Identify the blood parasite species.
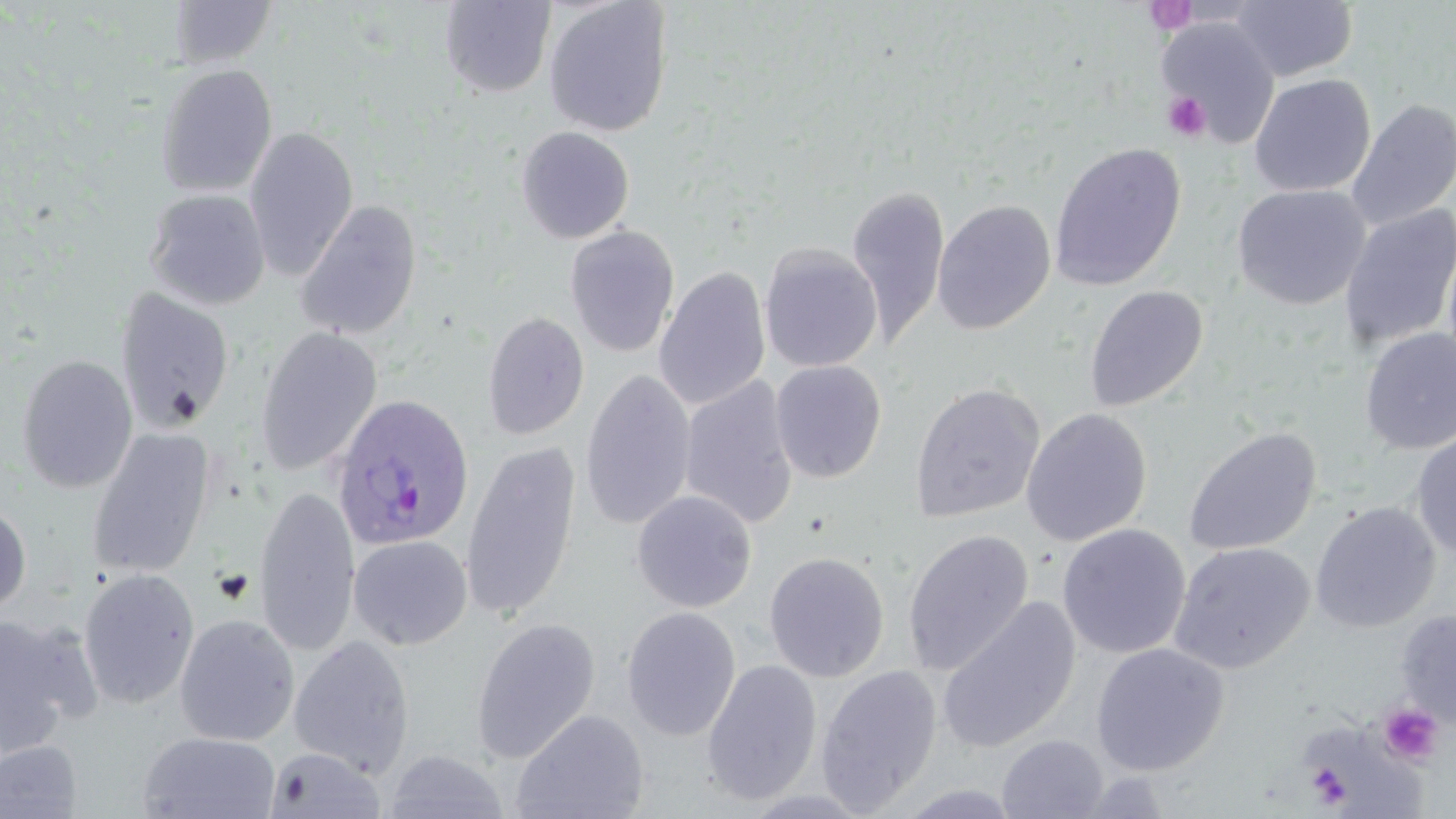

Plasmodium ovale.

image_size: 1456×819 pixels
magnification: 1000x
plasmodium_ovale_infected_red_blood_cell_locations: 'approximate bounding boxes as (x1,y1)-(x2,y2) corner pairs in pixels: (331,393)-(475,552)'
stain: May-Grünwald-Giemsa
preparation: thin blood film
platelet_locations: 'approximate bounding boxes as (x1,y1)-(x2,y2) corner pairs in pixels: (1163,91)-(1211,143), (1378,703)-(1444,765), (1305,762)-(1354,808)'
field_of_view: single
modality: light microscopy
uninfected_red_blood_cell_locations: 'approximate bounding boxes as (x1,y1)-(x2,y2) corner pairs in pixels: (439,0)-(556,98), (168,1)-(277,68), (543,1)-(673,138), (1229,1)-(1358,81), (1157,18)-(1279,146), (155,64)-(277,198), (1249,73)-(1375,197), (1346,98)-(1456,231), (244,126)-(358,282), (515,126)-(635,244), (1049,142)-(1187,292), (846,182)-(950,351), (1232,184)-(1371,310), (144,189)-(271,310), (932,199)-(1056,335), (295,200)-(423,340), (1338,205)-(1456,350), (565,226)-(681,358), (1442,234)-(1456,382), (758,242)-(883,373), (653,265)-(771,412), (1084,285)-(1209,412), (114,288)-(236,435), (481,310)-(589,441), (254,327)-(383,477), (1359,329)-(1456,455), (16,355)-(138,493), (770,360)-(887,483), (580,369)-(697,531), (679,375)-(800,529), (909,381)-(1046,523), (1021,407)-(1153,546), (1182,426)-(1322,557), (86,428)-(215,579), (1410,433)-(1456,560), (460,441)-(581,621), (254,485)-(360,658), (631,490)-(757,613), (0,501)-(31,617), (1310,502)-(1441,633), (1057,523)-(1191,659), (901,528)-(1034,677), (349,534)-(473,650), (1168,541)-(1314,674), (763,551)-(890,683), (77,569)-(200,709), (936,596)-(1082,756), (620,607)-(741,741), (1395,610)-(1456,731), (0,613)-(96,757), (174,614)-(300,747), (471,617)-(601,763), (288,634)-(414,778), (1091,643)-(1229,776), (701,659)-(823,806), (815,665)-(942,814), (510,708)-(650,819), (138,731)-(282,819), (997,734)-(1109,818), (0,740)-(81,818), (264,746)-(386,818), (384,749)-(512,819), (1073,771)-(1174,817)'